Assess for malaria.
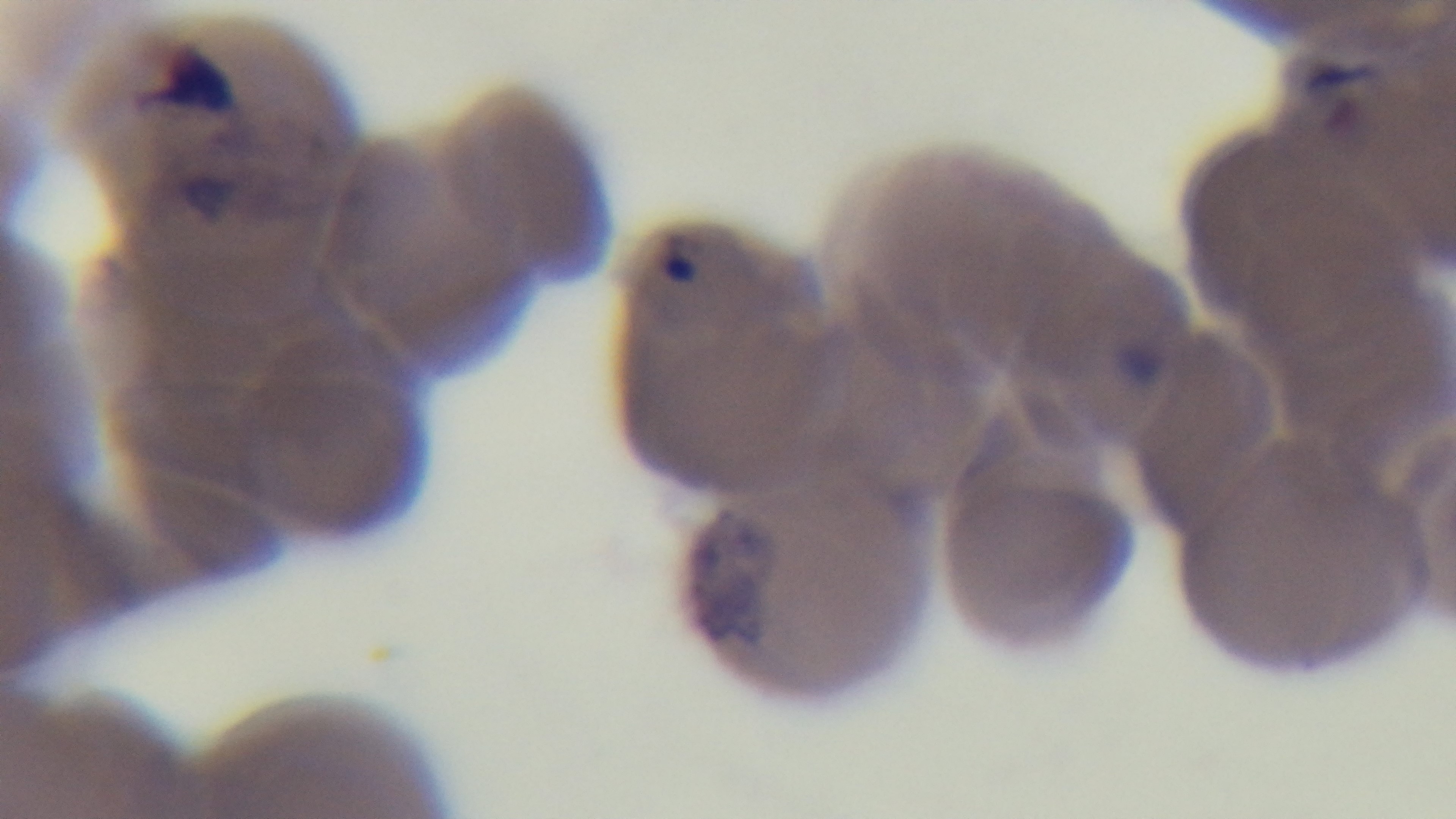
Positive.

stain: Giemsa
objective: 100x oil immersion
capture: mounted 4K digital camera
modality: light microscopy
field_of_view: one from the slide
preparation: thin blood film